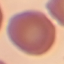

result: no malaria parasites seen
stain: Giemsa
preparation: thin smear
capture: smartphone camera at the microscope eyepiece
image_type: cell patch, automatically extracted from a larger field of view and resized to 64 × 64 pixels